Locate and identify every blood parasite.
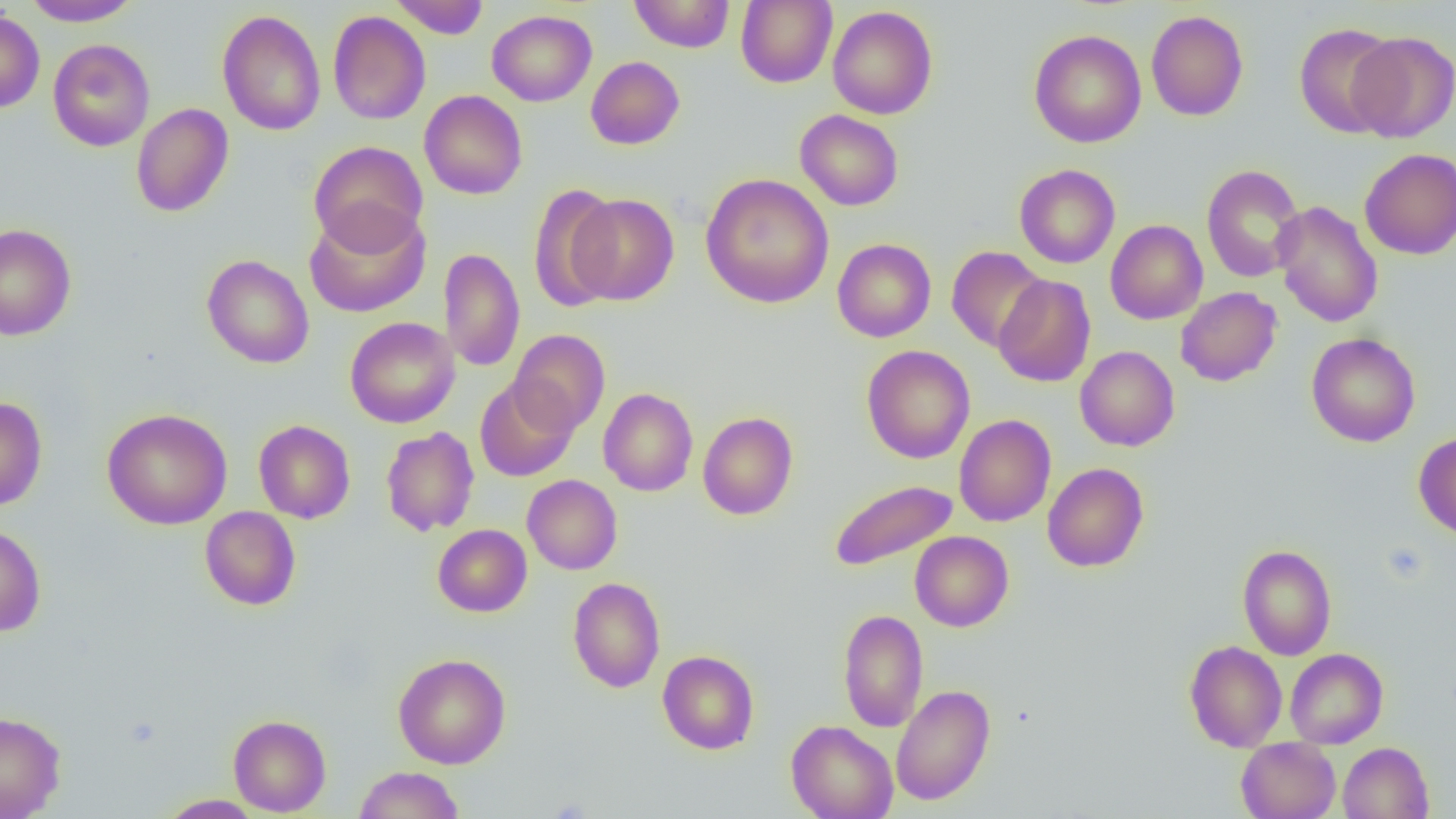

No blood parasites observed.

slide_level_diagnosis: no evidence of blood parasites
image_size: 1456×819 pixels
field_of_view: single
uninfected_red_blood_cell_locations: 'approximate bounding boxes as (x1, y1, x2, y2) in pixels: (22, 0, 143, 26), (390, 0, 489, 38), (629, 0, 735, 53), (735, 0, 837, 88), (827, 5, 938, 119), (217, 9, 326, 136), (0, 10, 45, 113), (328, 10, 430, 125), (487, 10, 597, 106), (1146, 10, 1248, 121), (1294, 22, 1401, 139), (1029, 29, 1146, 148), (1348, 31, 1456, 142), (48, 38, 155, 152), (586, 56, 685, 150), (419, 90, 528, 199), (131, 103, 234, 217), (795, 109, 904, 211), (308, 140, 429, 253), (1360, 148, 1456, 260), (1015, 164, 1120, 268), (1202, 164, 1305, 283), (700, 174, 834, 308), (528, 183, 622, 312), (569, 193, 679, 306), (1272, 200, 1383, 329), (304, 205, 431, 318), (1105, 220, 1208, 324), (0, 223, 76, 340), (832, 238, 936, 342), (947, 246, 1048, 352), (439, 248, 525, 372), (202, 254, 314, 368), (993, 275, 1096, 388), (1175, 287, 1282, 386), (344, 317, 459, 428), (509, 329, 611, 436), (1306, 332, 1420, 447), (861, 344, 975, 463), (1075, 346, 1180, 451), (474, 378, 578, 481), (598, 388, 698, 496), (0, 397, 48, 511), (102, 408, 232, 530), (697, 412, 798, 520), (954, 414, 1056, 527), (253, 419, 355, 523), (381, 426, 479, 536), (1414, 431, 1456, 542), (1042, 462, 1149, 572), (522, 474, 622, 575), (829, 478, 958, 572), (199, 506, 301, 611), (0, 523, 46, 636), (432, 524, 532, 617), (910, 531, 1014, 631), (1237, 544, 1337, 660), (567, 577, 665, 693), (838, 608, 928, 733), (1184, 640, 1287, 752), (1285, 648, 1388, 748), (658, 650, 759, 755), (393, 653, 510, 769), (891, 684, 995, 806), (0, 710, 66, 818), (228, 714, 331, 816), (786, 720, 898, 819), (1236, 738, 1340, 819), (1338, 742, 1433, 818), (353, 766, 465, 819), (157, 794, 264, 818)'
preparation: thin blood smear
magnification: 1000x
modality: optical microscopy
platelet_locations: 'approximate bounding boxes as (x1, y1, x2, y2) in pixels: (1381, 543, 1430, 583)'